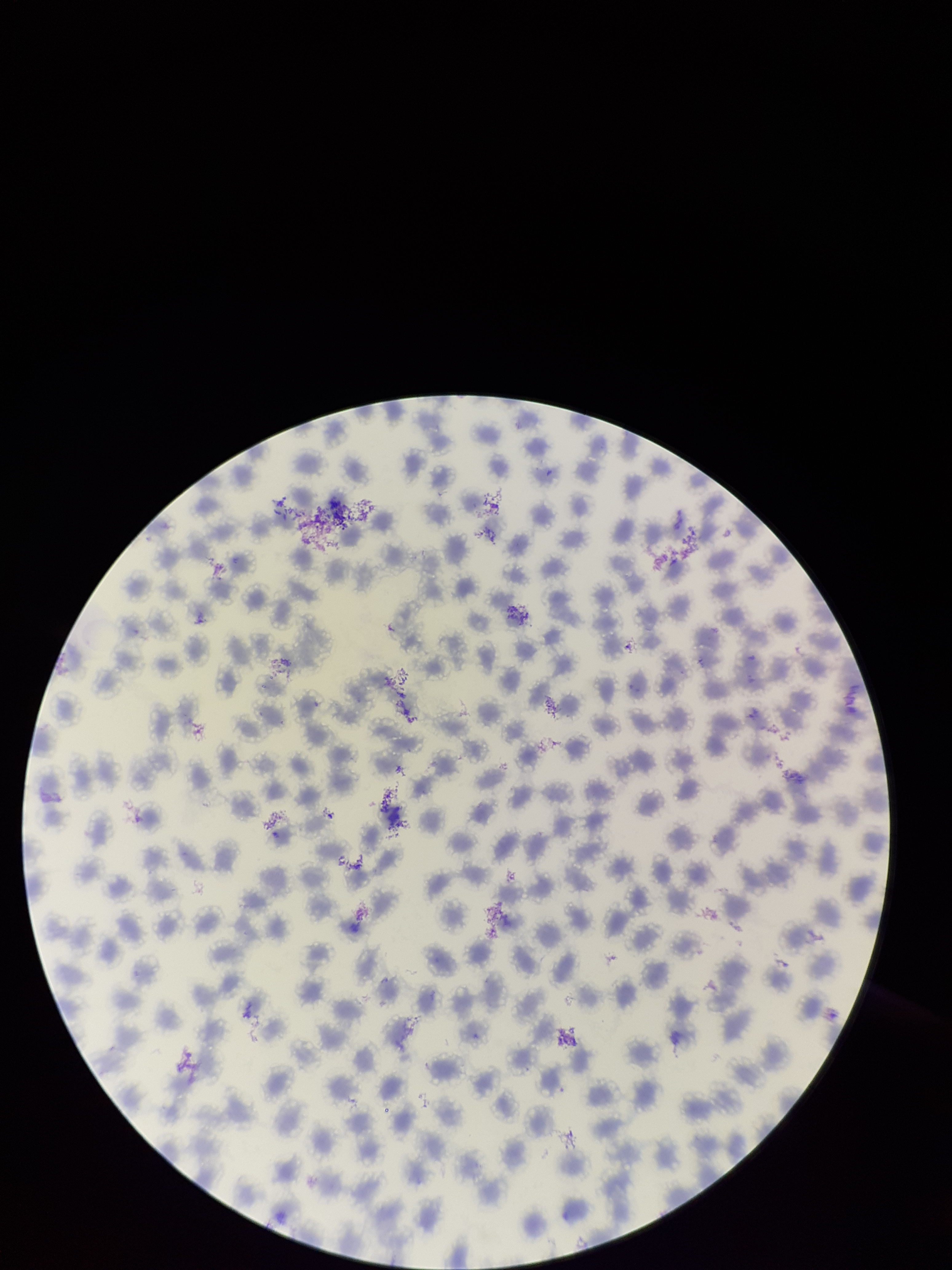
Image is 952×1270 pixels. Parasitized red blood cells: none seen. One field from this slide. Patient malaria status: positive. Preparation: thin smear. Smartphone photograph taken through the eyepiece of a microscope. Species reported for this patient: Plasmodium vivax. Parasitized red blood cell count: 0. Red blood cell count: 220. Stained with Giemsa.